Describe the morphology of the red blood cells.
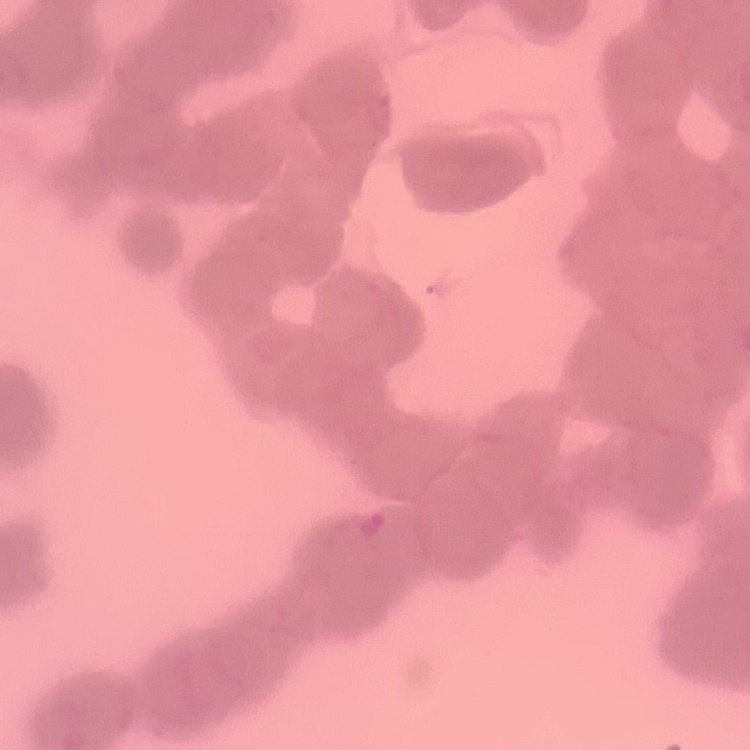
They show rouleaux formation.

Summary:
  - Image type: one tile cut from a larger photomicrograph
  - Stain: Field's or Giemsa
  - Preparation: thin blood smear